State which parasite is depicted.
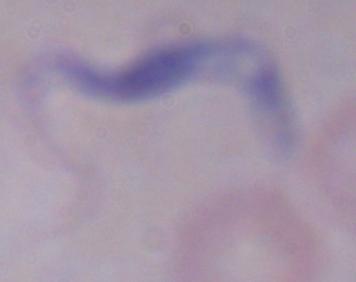
A trypanosome.

1000x magnification. Photomicrograph.